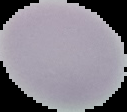

preparation: thin blood smear
image_type: cell region segmented out of the field of view; surrounding area masked to black
malaria_status: uninfected
image_size: 127×112 pixels